Name the cell type shown.
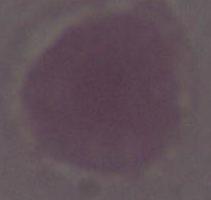

This is an erythrocyte.

Summary:
  - Modality: micrograph
  - Magnification: 1000x